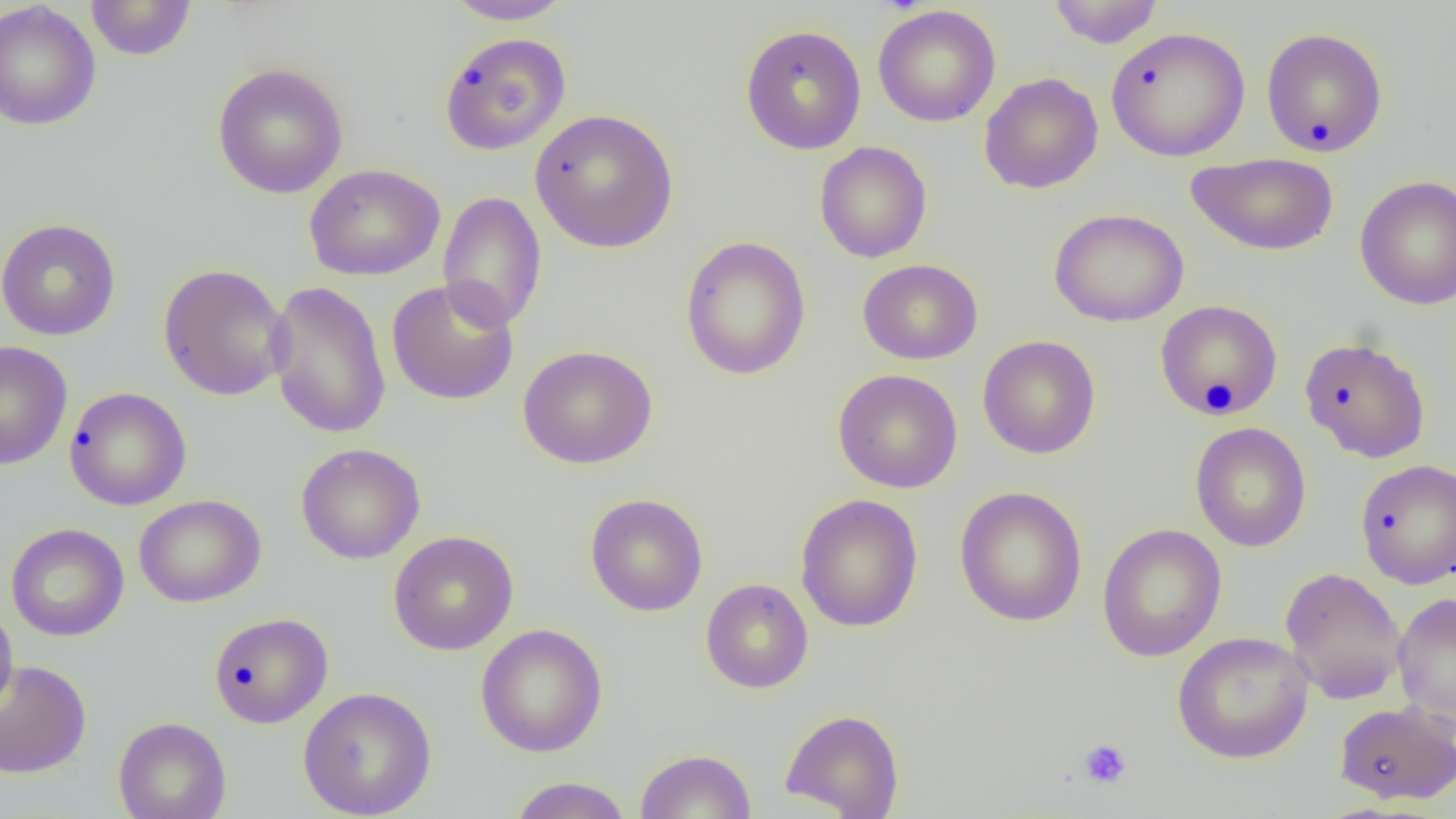
Approximate bounding boxes as (x1, y1, x2, y2) in pixels. Uninfected red blood cell locations: (85, 0, 198, 60), (442, 0, 576, 25), (1047, 0, 1165, 48), (0, 1, 101, 132), (873, 4, 1001, 127), (739, 24, 867, 155), (1106, 27, 1250, 162), (1260, 27, 1388, 157), (438, 32, 572, 156), (211, 62, 349, 199), (979, 72, 1103, 194), (529, 108, 679, 253), (814, 141, 932, 263), (1185, 152, 1339, 256), (305, 163, 445, 281), (1355, 175, 1456, 310), (437, 191, 547, 333), (1049, 208, 1189, 327), (0, 219, 121, 341), (680, 235, 811, 381), (857, 258, 983, 364), (157, 263, 291, 401), (386, 278, 520, 406), (265, 280, 392, 440), (1154, 299, 1284, 420), (978, 335, 1101, 459), (1299, 336, 1431, 463), (0, 340, 73, 470), (518, 345, 658, 469), (833, 368, 963, 493), (64, 386, 192, 511), (1190, 422, 1311, 552), (296, 443, 425, 564), (1354, 458, 1456, 589), (954, 485, 1088, 627), (585, 493, 708, 616), (795, 493, 924, 633), (133, 494, 266, 608), (6, 523, 129, 642), (1097, 523, 1227, 662), (388, 530, 518, 655), (1280, 566, 1408, 704), (700, 578, 813, 694), (1392, 592, 1456, 727), (0, 599, 18, 719), (209, 612, 333, 728), (475, 623, 608, 757), (1172, 631, 1315, 764), (0, 659, 92, 779), (297, 686, 437, 818), (1334, 701, 1455, 805), (780, 708, 905, 818), (113, 716, 232, 819), (634, 748, 758, 819), (507, 776, 633, 819). Platelet locations: (1078, 738, 1132, 790). Slide-level diagnosis: negative for blood parasites. One field of a larger specimen. Light microscopy. Image is 1456×819 pixels. 1000x magnification. Thin blood smear.